Comment on the morphology of the erythrocytes.
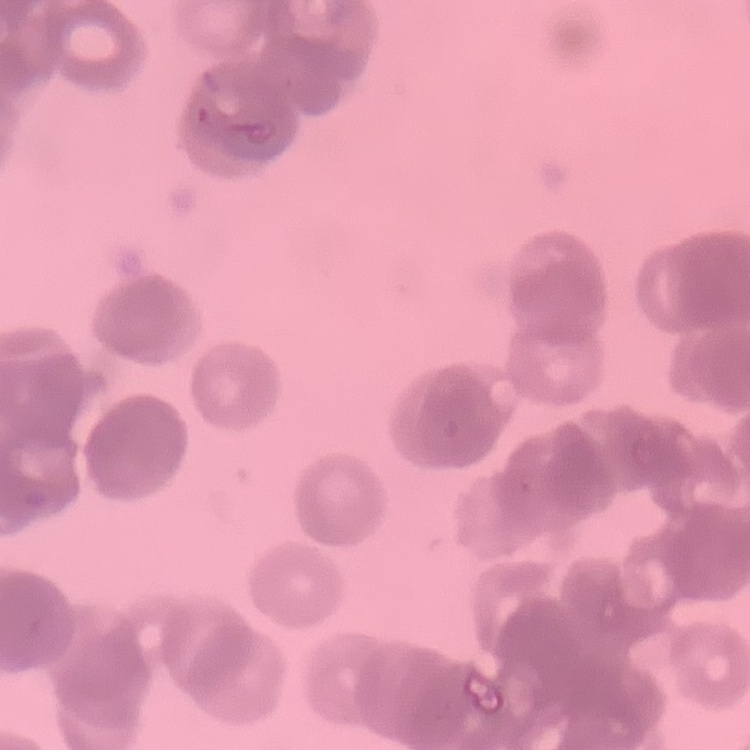
Rouleaux formation.

Summary:
  - Image type: square crop of a larger photomicrograph
  - Stain: Field's or Giemsa
  - Preparation: thin blood smear